Give the position of every Plasmodium parasite.
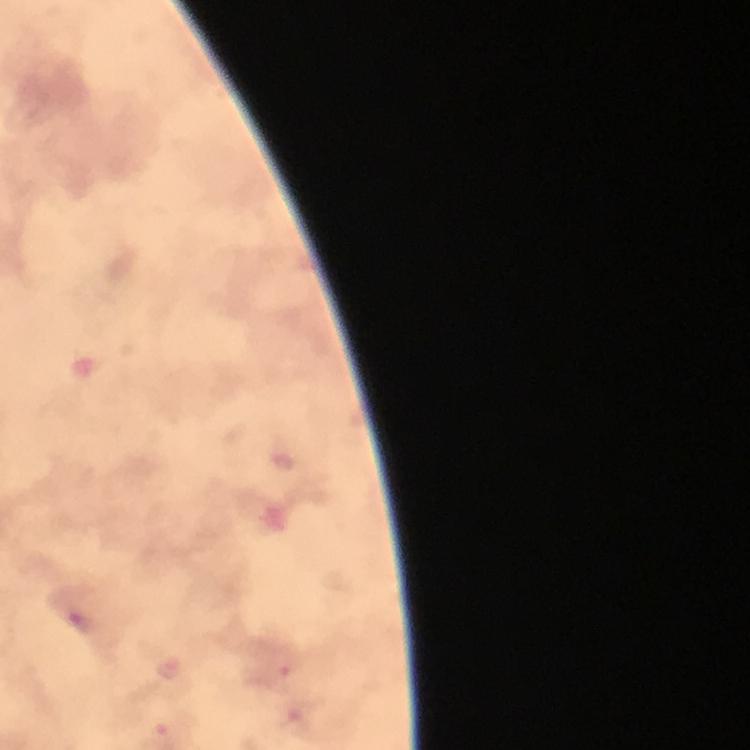
Approximate centers as [x, y] in pixels.
Plasmodium parasites: [81, 622], [170, 667], [275, 675].

At 100x magnification. From a diagnostic examination for malaria. Thick smear. Immersion oil was used. Giemsa-stained preparation. Smartphone photograph taken through a microscope. Cropped region of a single field of view. Image is 750×750 pixels.